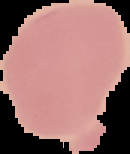
image size = 130×154 pixels
image type = segmented cell region with the area outside set to black
preparation = thin blood smear
malaria status = uninfected